Assess this cell for malaria.
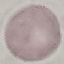
Uninfected.

Thin smear of blood. Giemsa-stained preparation. Automatically extracted cell patch, resized to 64 × 64 pixels. Acquired by smartphone through the microscope eyepiece.